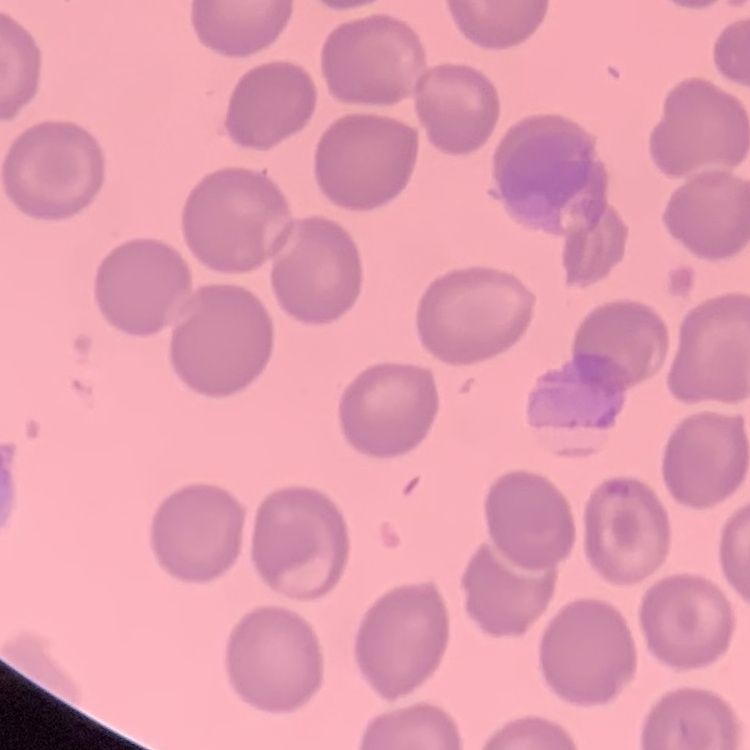
Summary:
  - Erythrocyte morphology: no rouleaux formation
  - Image type: one tile cut from a larger photomicrograph
  - Stain: Field's or Giemsa
  - Preparation: thin peripheral smear